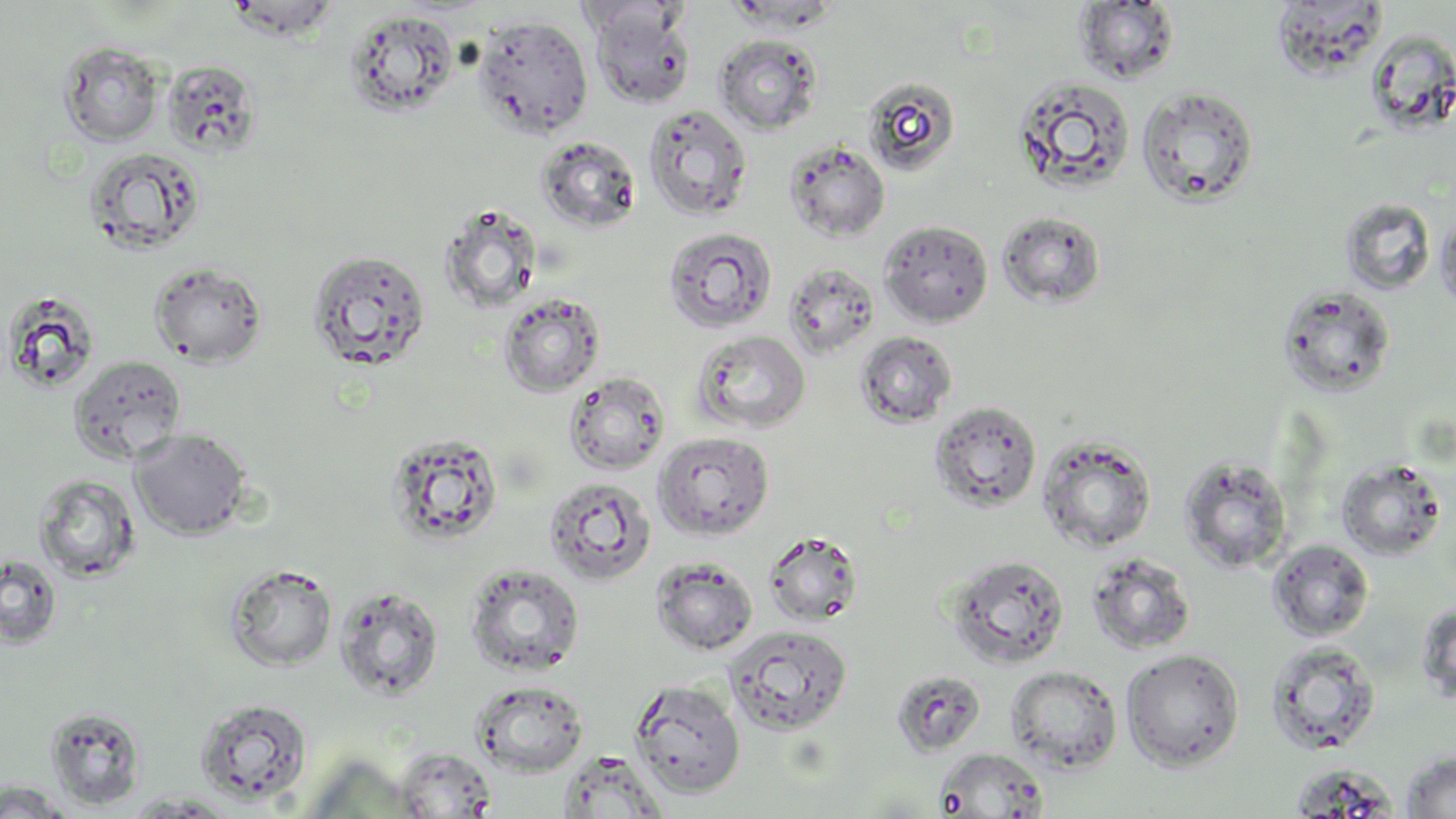

Summary:
  - Coordinate format: approximate bounding boxes as (x1, y1, x2, y2) in pixels
  - Uninfected red blood cell locations: (225, 0, 342, 42), (574, 1, 692, 41), (1074, 2, 1181, 84), (1268, 2, 1390, 78), (588, 5, 698, 110), (343, 9, 459, 117), (473, 14, 594, 139), (1365, 31, 1455, 141), (714, 34, 823, 135), (58, 41, 165, 145), (163, 61, 261, 156), (1012, 75, 1136, 196), (863, 76, 961, 176), (1137, 87, 1259, 207), (643, 103, 752, 220), (536, 135, 642, 233), (785, 140, 890, 242), (83, 146, 205, 256), (1339, 197, 1436, 296), (440, 204, 543, 313), (997, 210, 1106, 308), (1435, 210, 1456, 317), (879, 220, 994, 326), (662, 226, 777, 334), (308, 250, 431, 371), (149, 261, 267, 367), (783, 261, 880, 359), (1278, 284, 1397, 398), (2, 290, 102, 395), (498, 293, 605, 397), (693, 329, 810, 434), (854, 331, 958, 428), (68, 355, 187, 464), (564, 371, 671, 475), (930, 400, 1043, 512), (129, 428, 252, 540), (653, 431, 775, 540), (387, 432, 504, 546), (1037, 435, 1158, 552), (1179, 455, 1293, 574), (1336, 458, 1448, 561), (33, 474, 142, 582), (544, 476, 657, 586), (764, 531, 863, 627), (1267, 539, 1375, 642), (0, 553, 63, 649), (1087, 553, 1197, 655), (944, 554, 1070, 669), (650, 557, 758, 656), (225, 563, 337, 672), (464, 563, 585, 676), (334, 585, 444, 701), (1415, 601, 1456, 706), (724, 624, 853, 737), (1264, 640, 1382, 756), (1121, 648, 1245, 771), (1005, 665, 1123, 773), (891, 670, 987, 756), (629, 677, 746, 799), (471, 680, 589, 776), (193, 697, 313, 805), (44, 707, 146, 810), (395, 746, 498, 818), (934, 747, 1048, 818), (1400, 749, 1456, 818), (556, 750, 669, 818), (1287, 764, 1399, 816), (0, 781, 80, 818), (121, 792, 242, 817)
  - Slide-level diagnosis: negative for blood parasites
  - Preparation: thin blood smear
  - Magnification: 1000x
  - Stain: May-Grünwald-Giemsa
  - Image size: 1456×819 pixels
  - Modality: optical microscopy
  - Field of view: one of a larger specimen